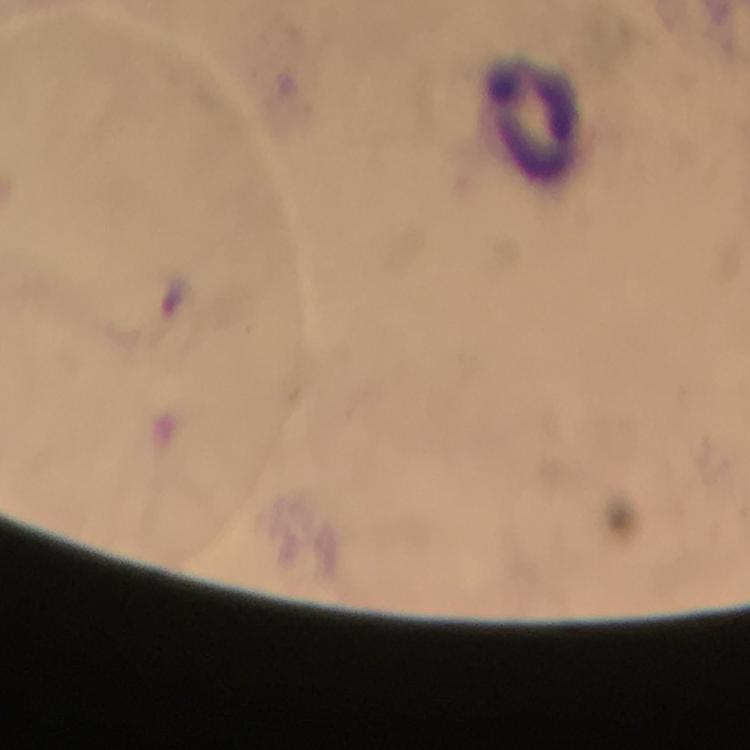

Approximate object centers, in pixels from the top-left corner. Leukocyte locations: (x=537, y=117). Immersion oil applied. Malaria parasites: none seen. Thick smear. Smartphone photograph taken through a microscope. Giemsa-stained preparation. Image is 750×750 pixels. From a diagnostic examination for malaria. Cropped region of a single field of view. 100x magnification.